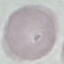

Summary:
  - Result: no malaria parasites seen
  - Stain: Giemsa
  - Capture: smartphone through the microscope eyepiece
  - Preparation: thin blood film
  - Image type: automatically extracted cell patch, resized to 64 × 64 pixels